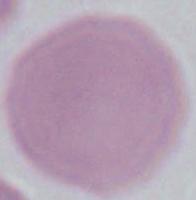 1000x magnification. Photomicrograph. A red blood cell is shown.